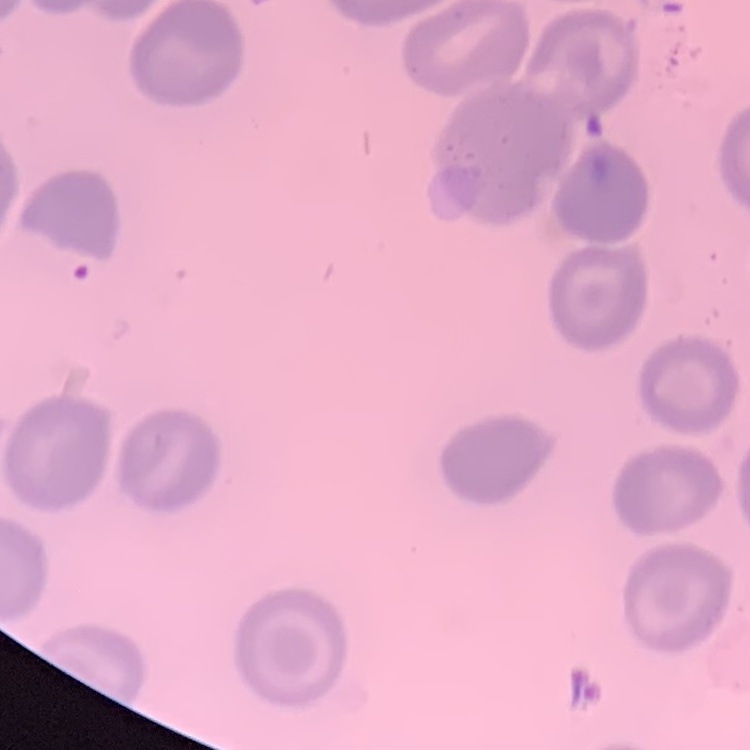

erythrocyte morphology = no rouleaux formation
stain = Field's or Giemsa
image type = one tile cut from a larger photomicrograph
preparation = thin blood film